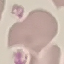
Malaria status: uninfected. Automatically extracted cell patch, resized to 64 × 64 pixels. Thin smear of blood. Giemsa stain. Acquired by smartphone through the microscope eyepiece.